Name the parasite shown.
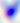

Toxoplasma gondii.

magnification = 400x
modality = photomicrograph